Identify the parasite.
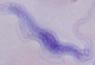
A trypanosome.

1000x magnification. Micrograph.